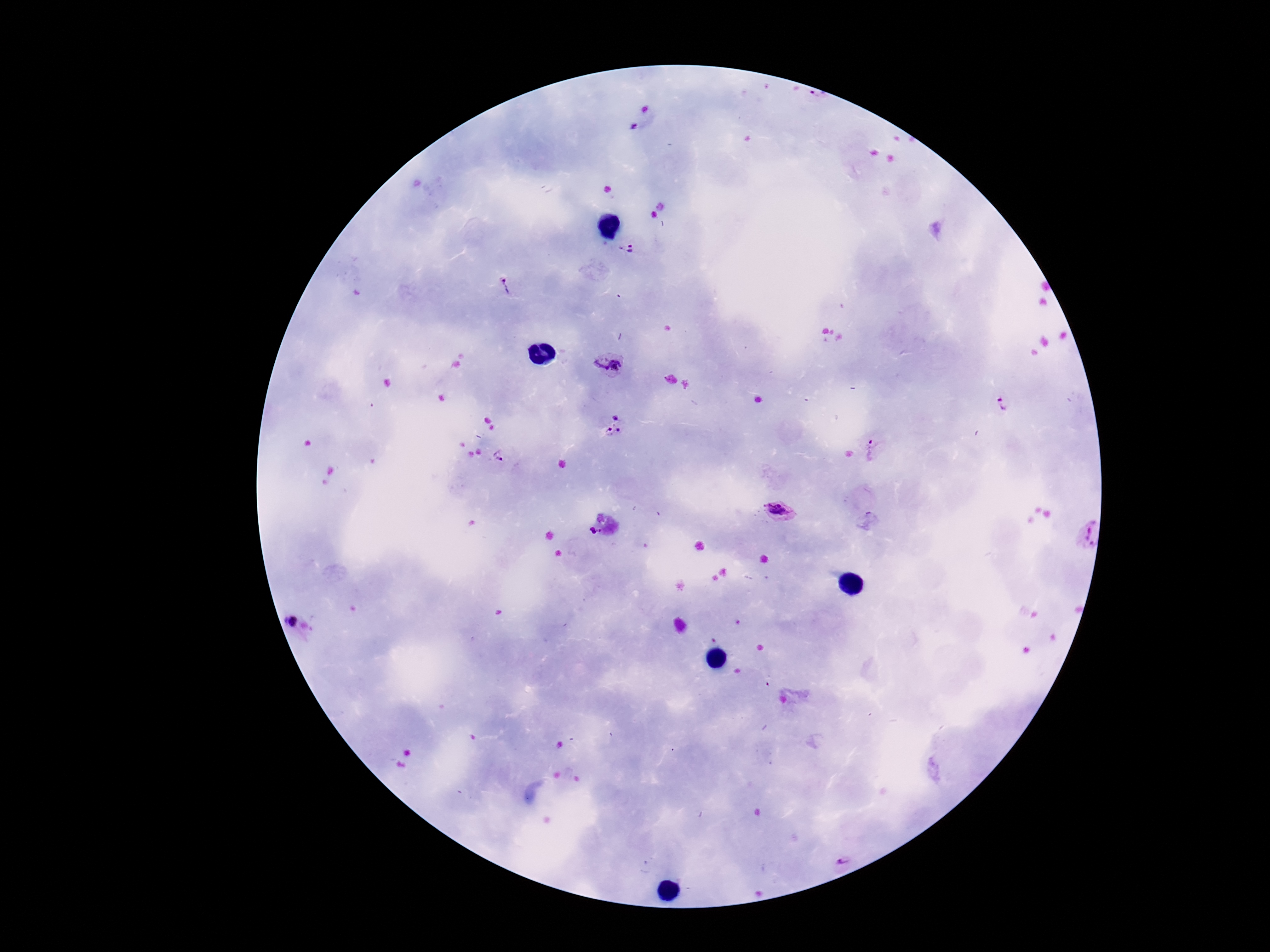

Approximate centers as [x, y] in pixels. Plasmodium parasite locations: [632, 249], [506, 287], [609, 364], [1001, 404], [615, 427], [870, 446], [498, 456], [781, 511], [596, 532], [1081, 533], [299, 624], [841, 853]. Patient malaria status: infected. Image is 1270×952 pixels. Single field of view. Smartphone photograph taken through the microscope eyepiece. Giemsa stain. Thick peripheral-blood smear. 100x magnification.